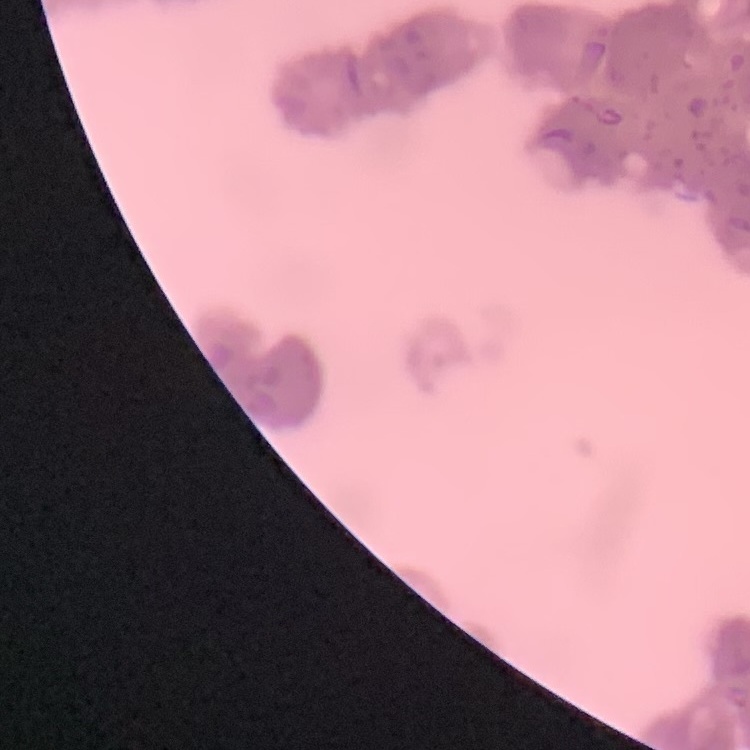
Summary:
  - Red blood cell morphology: rouleaux formation
  - Stain: Field's or Giemsa
  - Preparation: thin peripheral smear
  - Image type: one tile cut from a larger photomicrograph